Point out each leukocyte.
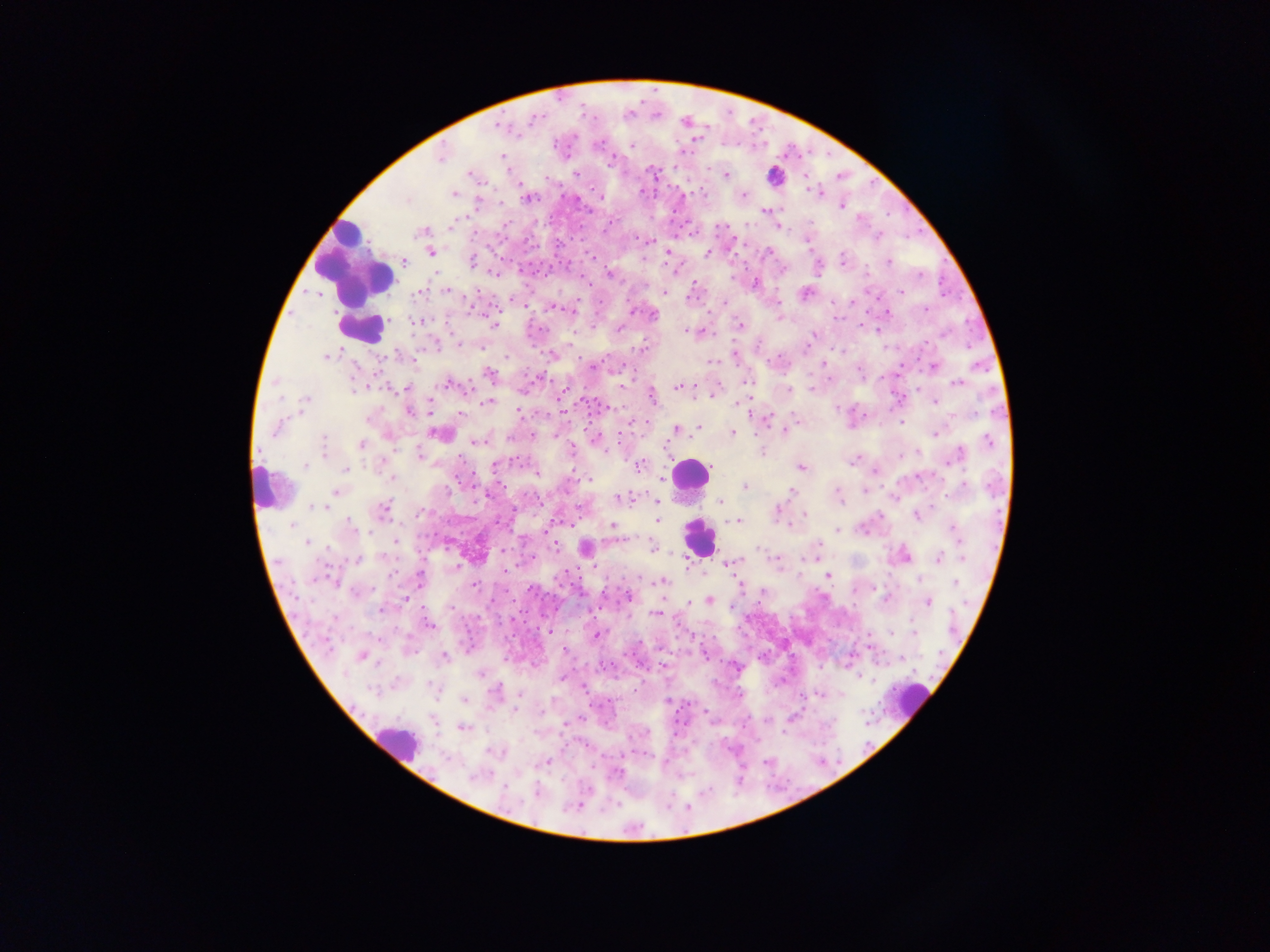

Approximate centers as (x, y) in pixels.
Leukocytes: (775, 176), (353, 263), (361, 329), (689, 474), (265, 490), (697, 537), (911, 701), (396, 741).

image_size: 1270×952 pixels
preparation: thick blood film
country: Ghana
capture: mobile-phone photograph through a microscope
field_of_view: single
malaria_parasite_locations: 'approximate centers as (x, y) in pixels: (533, 120), (499, 126), (599, 144), (632, 146), (440, 156), (503, 157), (576, 173), (471, 175), (726, 175), (455, 193), (744, 195), (601, 197), (528, 198), (406, 199), (478, 203), (842, 206), (766, 211), (452, 225), (420, 232), (431, 252), (707, 253), (842, 260), (405, 262), (471, 262), (889, 262), (608, 275), (755, 284), (446, 292), (664, 292), (902, 292), (420, 293), (805, 293), (512, 300), (724, 303), (552, 308), (925, 309), (888, 312), (653, 316), (417, 320), (493, 324), (739, 325), (620, 328), (686, 332), (814, 334), (943, 335), (459, 344), (640, 348), (735, 355), (327, 356), (713, 361), (593, 366), (933, 366), (489, 373), (958, 383), (449, 384), (678, 387), (354, 389), (407, 389), (788, 389), (714, 393), (652, 396), (306, 399), (488, 402), (934, 403), (737, 404), (409, 411), (520, 412), (460, 413), (368, 419), (902, 422), (699, 427), (277, 428), (676, 429), (784, 431), (733, 433), (438, 434), (935, 434), (324, 440), (476, 441), (989, 441), (362, 444), (571, 450), (762, 451), (917, 452), (324, 454), (958, 454), (420, 455), (853, 461), (640, 465), (305, 466), (494, 467), (800, 467), (347, 468), (875, 471), (537, 474), (392, 477), (588, 480), (744, 487), (961, 487), (865, 491), (790, 492), (335, 493), (838, 494), (620, 498), (841, 498), (656, 502), (720, 502), (314, 507), (321, 507), (384, 508), (776, 512), (420, 513), (805, 515), (917, 515), (657, 521), (737, 521), (350, 523), (292, 525), (612, 525), (839, 530), (955, 532), (396, 541), (307, 543), (818, 544), (556, 546), (653, 546), (586, 549), (760, 549), (939, 557), (777, 559), (357, 560), (729, 563), (456, 567), (505, 571), (393, 573), (829, 575), (420, 578), (920, 579), (661, 582), (956, 582), (473, 586), (354, 593), (627, 596), (886, 597), (406, 600), (710, 600), (928, 602), (689, 603), (452, 609), (380, 611), (656, 613), (429, 625), (548, 631), (893, 632), (913, 632), (596, 636), (565, 650), (361, 656), (444, 657), (479, 673), (345, 674), (496, 689), (371, 690), (464, 699), (514, 709), (463, 728), (547, 762), (618, 773), (475, 776), (505, 788), (536, 791)'